Locate and identify every blood parasite.
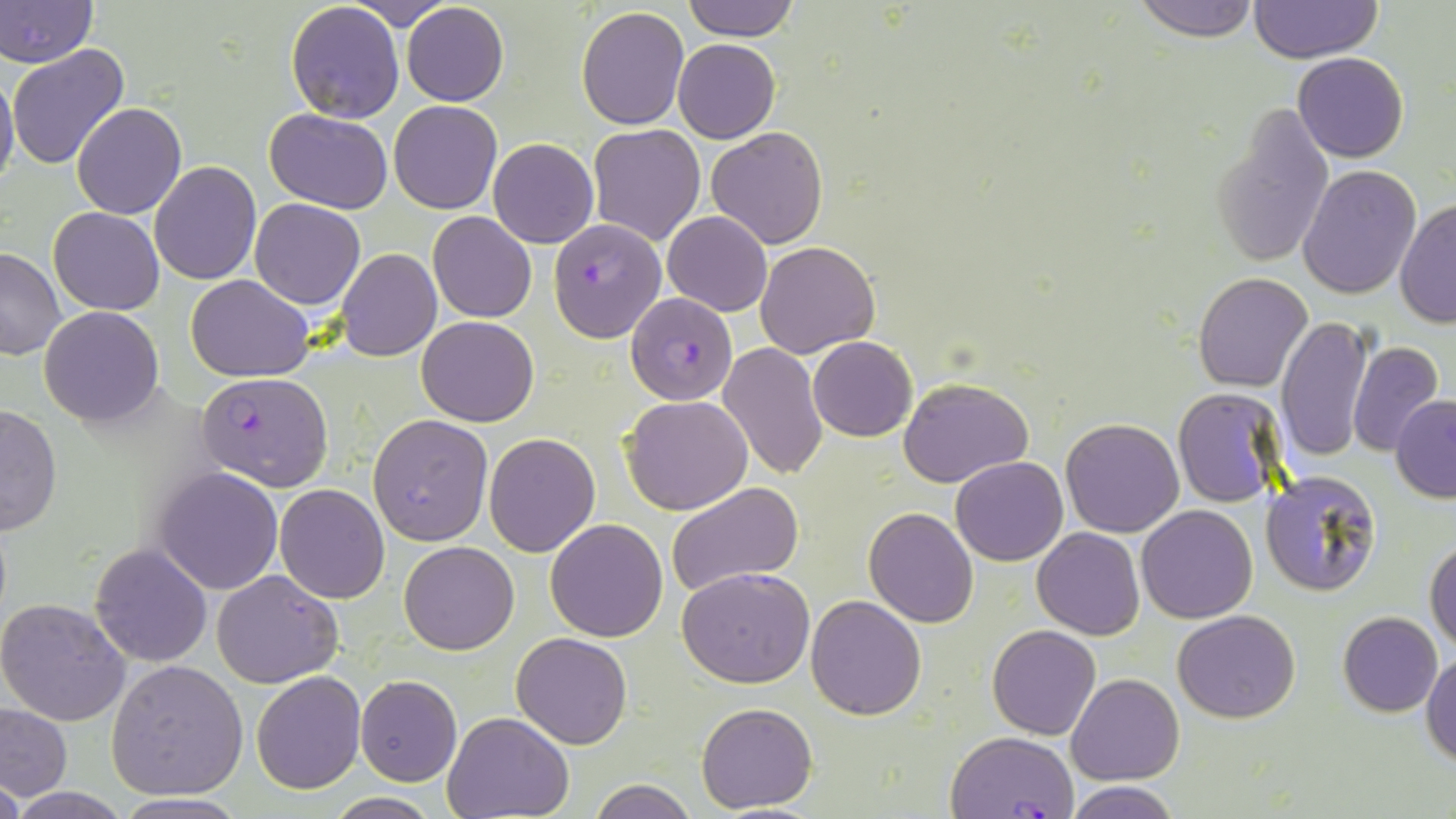

Approximate bounding boxes as named x1/y1/x2/y2 corners in pixels.
Plasmodium falciparum-infected red blood cells: (x1=547, y1=218, x2=667, y2=341), (x1=626, y1=292, x2=737, y2=404), (x1=198, y1=371, x2=332, y2=491), (x1=949, y1=731, x2=1080, y2=819).
No Plasmodium ovale, Plasmodium malariae, Plasmodium vivax, Babesia divergens, or Trypanosoma brucei observed.

Uninfected red blood cell locations: (x1=1, y1=0, x2=98, y2=67), (x1=344, y1=0, x2=456, y2=29), (x1=682, y1=0, x2=800, y2=41), (x1=1133, y1=0, x2=1262, y2=41), (x1=1249, y1=0, x2=1382, y2=64), (x1=285, y1=1, x2=405, y2=125), (x1=402, y1=3, x2=508, y2=106), (x1=574, y1=7, x2=690, y2=129), (x1=673, y1=39, x2=779, y2=144), (x1=7, y1=44, x2=130, y2=170), (x1=1293, y1=52, x2=1408, y2=162), (x1=0, y1=69, x2=19, y2=197), (x1=72, y1=101, x2=187, y2=219), (x1=389, y1=101, x2=502, y2=215), (x1=1212, y1=103, x2=1335, y2=269), (x1=265, y1=107, x2=394, y2=212), (x1=588, y1=123, x2=705, y2=246), (x1=706, y1=126, x2=828, y2=250), (x1=488, y1=137, x2=599, y2=249), (x1=150, y1=162, x2=261, y2=285), (x1=1299, y1=165, x2=1422, y2=298), (x1=249, y1=198, x2=366, y2=309), (x1=1395, y1=198, x2=1456, y2=328), (x1=48, y1=207, x2=163, y2=314), (x1=662, y1=211, x2=772, y2=316), (x1=428, y1=212, x2=537, y2=324), (x1=755, y1=241, x2=879, y2=358), (x1=0, y1=248, x2=66, y2=360), (x1=336, y1=248, x2=441, y2=361), (x1=1192, y1=273, x2=1313, y2=392), (x1=186, y1=275, x2=314, y2=381), (x1=38, y1=306, x2=164, y2=426), (x1=1277, y1=315, x2=1372, y2=463), (x1=417, y1=316, x2=539, y2=426), (x1=807, y1=336, x2=917, y2=441), (x1=1348, y1=342, x2=1444, y2=455), (x1=719, y1=343, x2=827, y2=481), (x1=899, y1=376, x2=1033, y2=489), (x1=1172, y1=388, x2=1287, y2=507), (x1=622, y1=395, x2=753, y2=515), (x1=1392, y1=395, x2=1456, y2=500), (x1=0, y1=402, x2=61, y2=539), (x1=368, y1=413, x2=493, y2=545), (x1=1062, y1=417, x2=1184, y2=538), (x1=483, y1=432, x2=600, y2=557), (x1=951, y1=455, x2=1068, y2=566), (x1=153, y1=467, x2=285, y2=594), (x1=1259, y1=469, x2=1382, y2=596), (x1=667, y1=482, x2=804, y2=600), (x1=275, y1=484, x2=390, y2=603), (x1=1137, y1=504, x2=1257, y2=622), (x1=864, y1=508, x2=979, y2=627), (x1=544, y1=518, x2=669, y2=641), (x1=1032, y1=528, x2=1144, y2=641), (x1=1425, y1=536, x2=1456, y2=653), (x1=399, y1=540, x2=521, y2=655), (x1=90, y1=544, x2=211, y2=666), (x1=676, y1=566, x2=814, y2=688), (x1=212, y1=568, x2=343, y2=687), (x1=806, y1=594, x2=927, y2=720), (x1=0, y1=596, x2=131, y2=726), (x1=1172, y1=609, x2=1301, y2=723), (x1=1338, y1=611, x2=1442, y2=716), (x1=987, y1=624, x2=1101, y2=740), (x1=512, y1=632, x2=633, y2=749), (x1=1422, y1=651, x2=1455, y2=766), (x1=106, y1=659, x2=249, y2=800), (x1=250, y1=671, x2=366, y2=795), (x1=354, y1=675, x2=463, y2=786), (x1=1066, y1=675, x2=1182, y2=786), (x1=697, y1=702, x2=818, y2=813), (x1=0, y1=703, x2=73, y2=802), (x1=443, y1=713, x2=574, y2=819), (x1=587, y1=778, x2=699, y2=819), (x1=1068, y1=781, x2=1180, y2=819), (x1=324, y1=793, x2=443, y2=818). Slide-level diagnosis: Plasmodium falciparum. May-Grünwald-Giemsa stain. Captured at 1000x magnification. Image is 1456×819 pixels. Single field of view. Thin blood film. Optical microscopy.